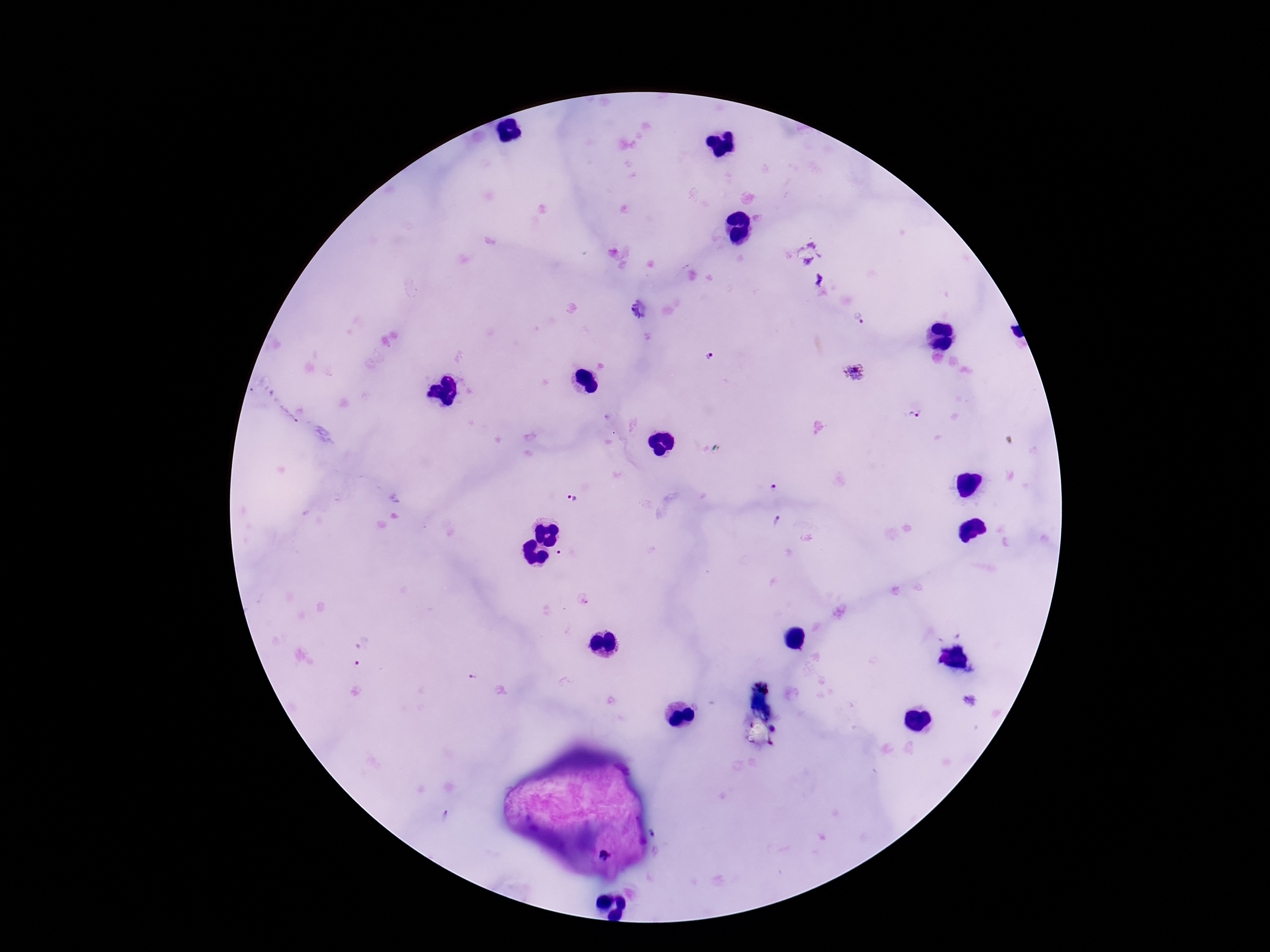
{
  "magnification": "100x",
  "patient_malaria_status": "positive",
  "plasmodium_parasite_locations": "approximate centers as (x, y) in pixels: (818, 278), (859, 319), (711, 357), (855, 373), (916, 416), (773, 488), (572, 499), (777, 520), (558, 554), (360, 652), (472, 679)",
  "image_size": "1270×952 pixels",
  "field_of_view": "single",
  "capture": "smartphone camera through the microscope eyepiece",
  "preparation": "thick peripheral-blood smear",
  "stain": "Giemsa"
}